Report the malaria status of this cell.
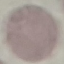

Uninfected.

Summary:
  - Stain: Giemsa
  - Image type: automatically extracted cell patch, resized to 64 × 64 pixels
  - Preparation: thin smear
  - Capture: smartphone through the microscope eyepiece